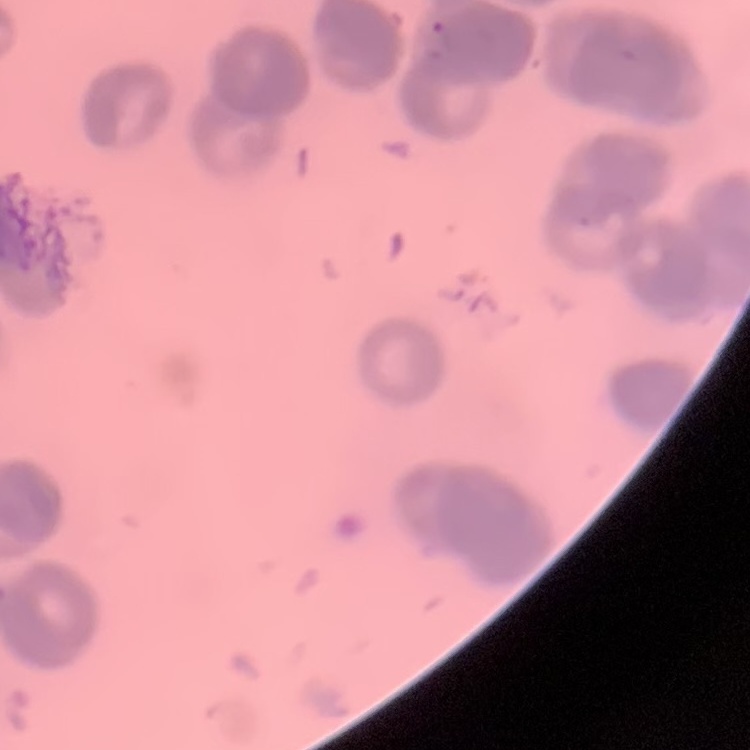

red blood cell morphology = rouleaux formation
stain = Field's or Giemsa
image type = one tile cut from a larger photomicrograph
preparation = thin blood film